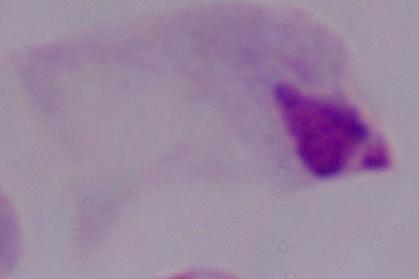
magnification = 1000x
identification = trichomonad
modality = photomicrograph